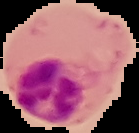
From a thin blood film. Result: malaria parasites identified. Segmented cell region on a black background. Image is 139×133 pixels.